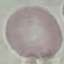

{
  "malaria_status": "uninfected",
  "image_type": "cell patch, automatically extracted from a larger field of view and resized to 64 × 64 pixels",
  "preparation": "thin blood smear",
  "stain": "Giemsa",
  "capture": "smartphone through the microscope eyepiece"
}